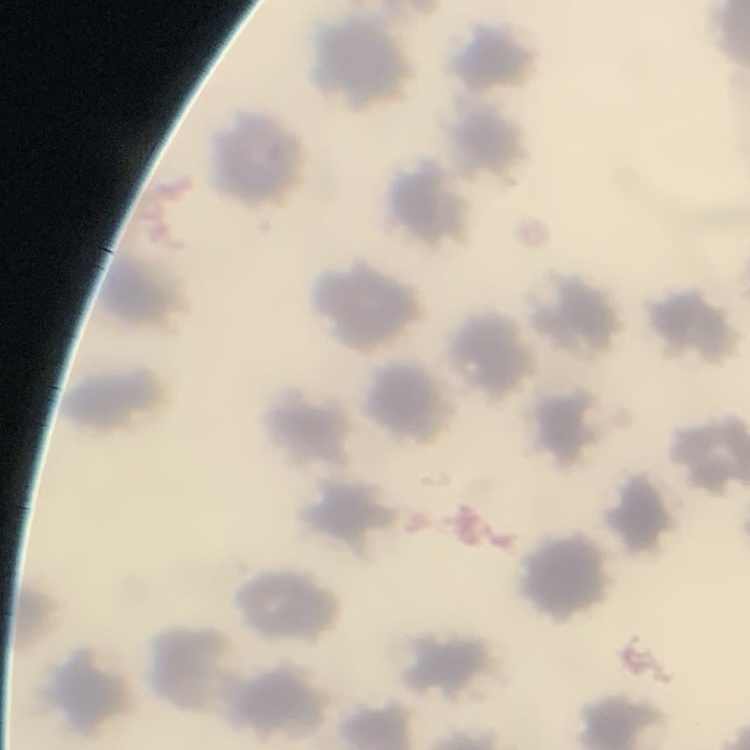 The erythrocytes exhibit no rouleaux formation. Thin blood film. Square crop of a larger photomicrograph. Field's or Giemsa stain.